Assess this cell for malaria.
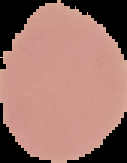

Uninfected.

image type = cell region segmented out of the field of view; surrounding area masked to black
preparation = thin blood film
image size = 127×163 pixels